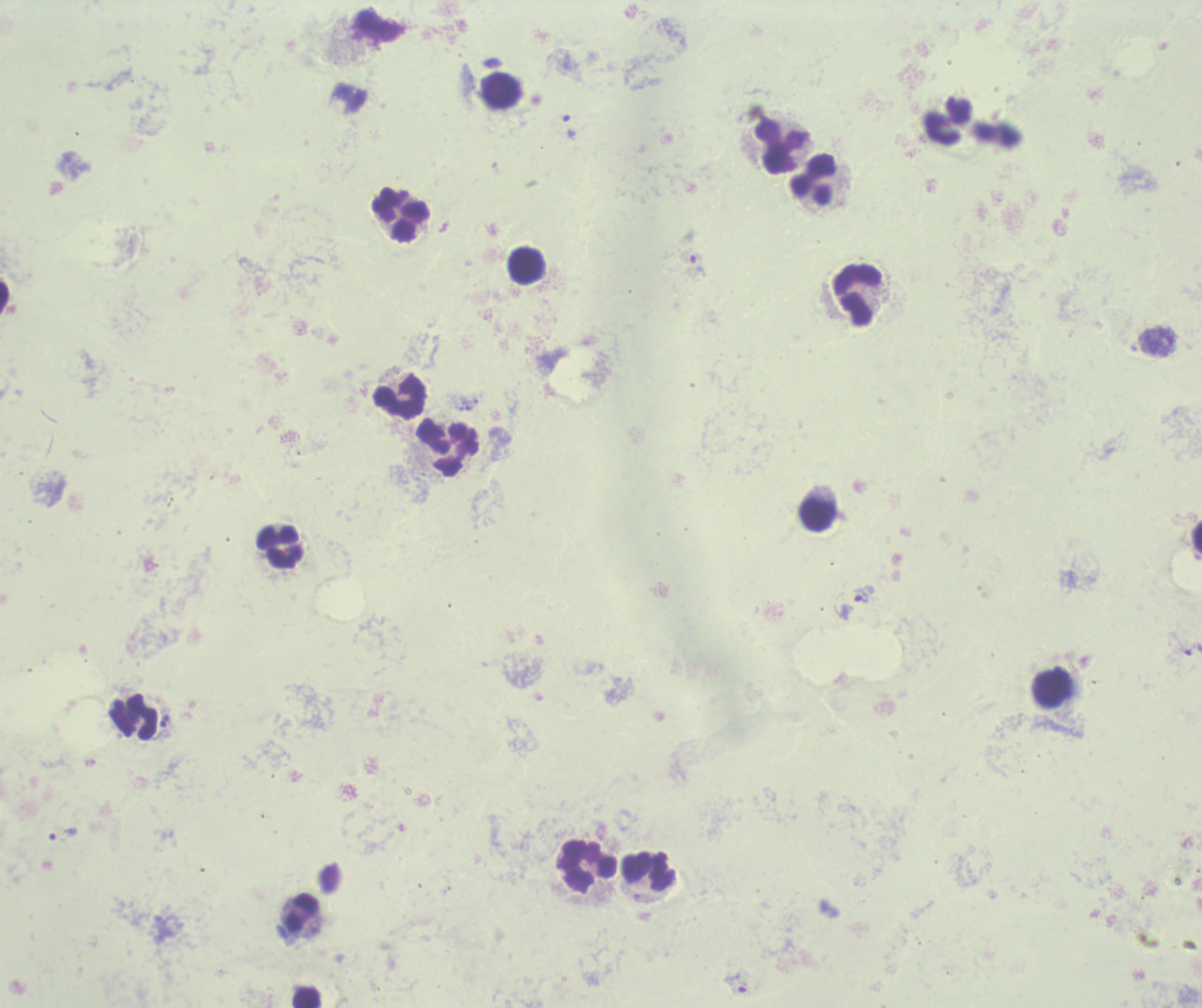
Approximate centers as (x, y) in pixels.
Summary:
  - Leukocyte locations: (500, 90), (780, 147), (813, 179), (400, 215), (525, 266), (856, 294), (399, 398), (447, 446), (819, 515), (1196, 536), (279, 548), (1053, 689), (134, 719), (588, 865), (649, 872), (303, 913), (306, 997)
  - Trophozoite locations: (699, 266), (863, 594), (1192, 649), (166, 721), (63, 834), (736, 983)
  - Stain: Romanowsky
  - Result: malaria parasites identified
  - Context: previously used in an actual diagnosis
  - Image size: 1202×1008 pixels
  - Magnification: 100x
  - Preparation: thick blood smear
  - Field of view: single
  - Background quality: unsatisfactory